Comment on the morphology of the red blood cells.
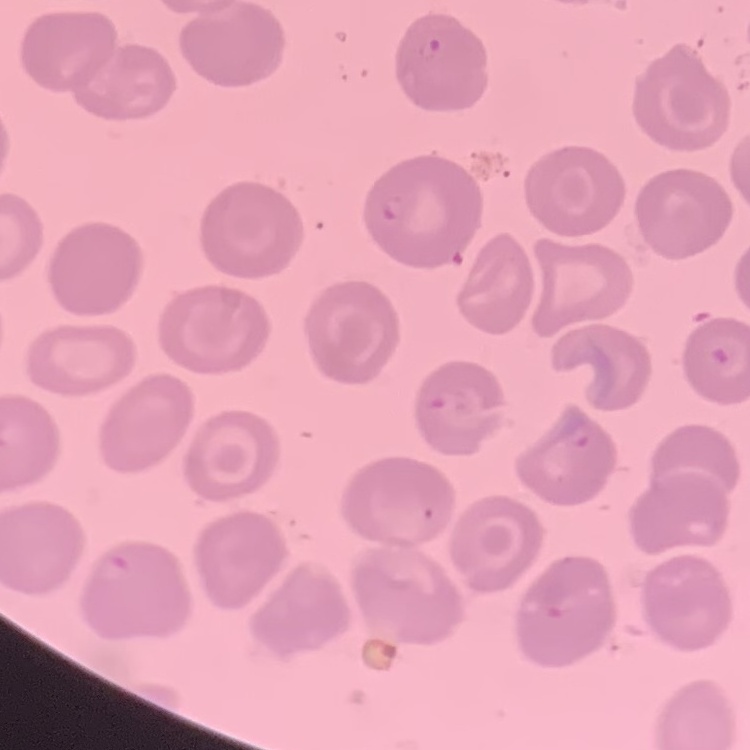
No rouleaux formation.

{
  "stain": "Field's or Giemsa",
  "image_type": "square crop of a larger photomicrograph",
  "preparation": "thin blood film"
}